Outline each Plasmodium falciparum-infected red blood cell.
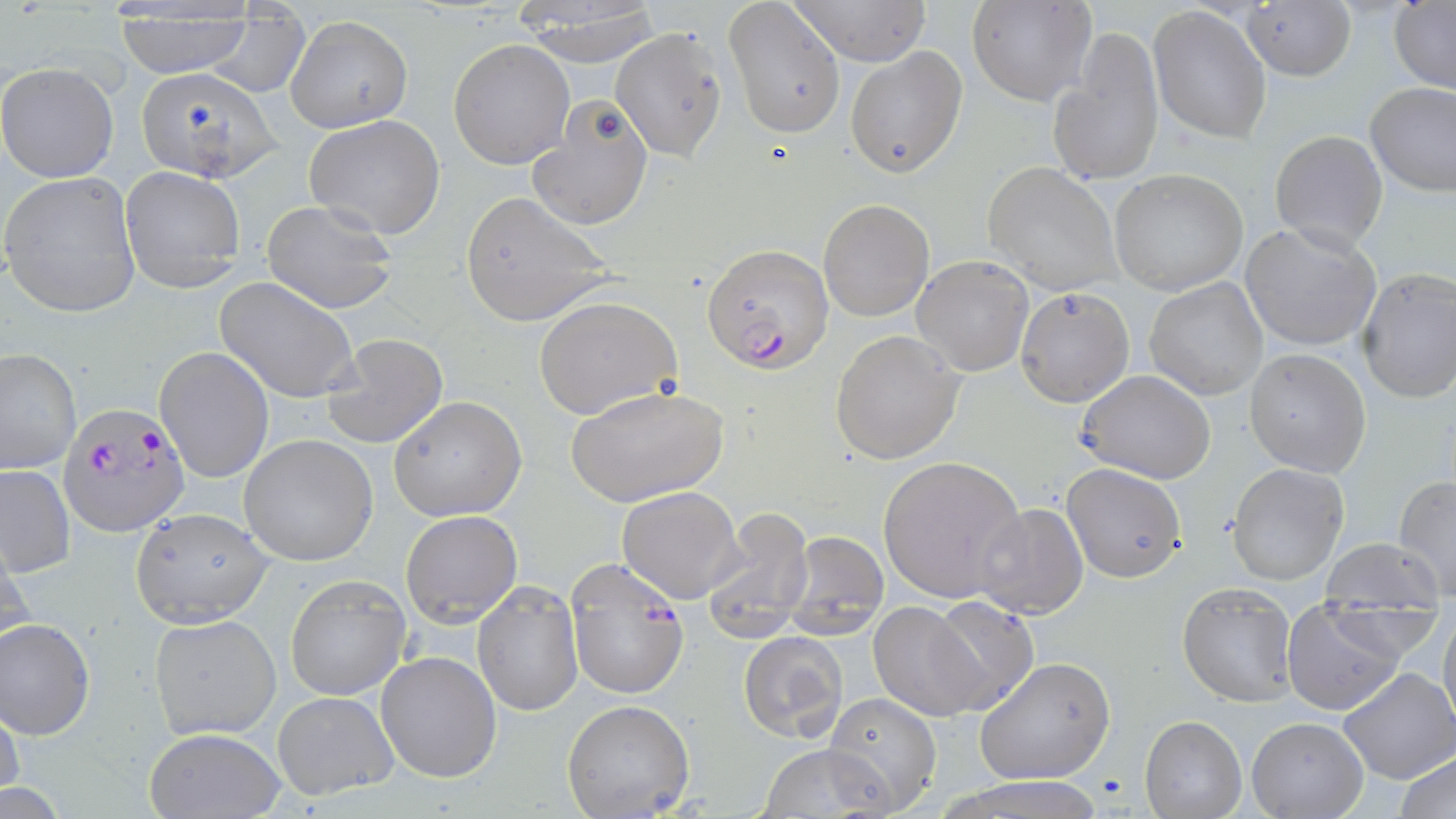

Approximate bounding boxes as (x1, y1, x2, y2) in pixels.
Plasmodium falciparum-infected red blood cells: (702, 245, 832, 372), (58, 403, 190, 537), (566, 558, 690, 699).

slide-level diagnosis = Plasmodium falciparum
image size = 1456×819 pixels
field of view = one of a larger specimen
magnification = 1000x
preparation = thin blood smear
uninfected red blood cell locations = approximate bounding boxes as (x1, y1, x2, y2) in pixels: (723, 0, 846, 135), (792, 0, 930, 64), (969, 0, 1096, 107), (1241, 0, 1356, 82), (509, 2, 667, 65), (1391, 2, 1456, 92), (1148, 4, 1272, 145), (203, 5, 311, 97), (111, 13, 256, 79), (286, 15, 412, 131), (611, 26, 729, 162), (1050, 27, 1165, 189), (449, 39, 575, 169), (844, 44, 968, 179), (1, 62, 119, 183), (137, 66, 279, 183), (1364, 81, 1456, 198), (527, 99, 654, 232), (302, 114, 447, 240), (1269, 130, 1389, 252), (982, 162, 1122, 294), (119, 166, 246, 293), (1109, 168, 1247, 296), (1, 172, 141, 318), (458, 192, 613, 326), (818, 199, 934, 321), (262, 204, 398, 298), (1241, 223, 1383, 352), (911, 255, 1034, 375), (1356, 268, 1456, 404), (215, 277, 359, 404), (1144, 277, 1269, 401), (1016, 287, 1131, 407), (535, 296, 681, 421), (829, 329, 967, 464), (324, 333, 449, 449), (0, 348, 80, 473), (156, 348, 272, 483), (1244, 348, 1370, 476), (1077, 369, 1217, 485), (565, 383, 729, 510), (389, 395, 529, 521), (239, 435, 378, 566), (877, 455, 1025, 602), (1061, 462, 1187, 584), (1229, 463, 1348, 584), (0, 465, 74, 578), (1393, 474, 1456, 600), (617, 485, 746, 602), (972, 501, 1087, 620), (129, 508, 274, 628), (699, 509, 816, 628), (400, 510, 522, 626), (782, 530, 888, 632), (1, 533, 33, 652), (1320, 538, 1442, 621), (284, 573, 412, 700), (473, 581, 583, 717), (1177, 582, 1298, 707), (921, 595, 1041, 714), (1281, 598, 1404, 716), (869, 601, 991, 722), (1439, 607, 1456, 737), (149, 613, 282, 741), (0, 618, 95, 739), (737, 631, 849, 744), (376, 651, 502, 783), (974, 656, 1116, 786), (1338, 667, 1455, 784), (271, 691, 399, 801), (823, 693, 942, 815), (562, 700, 695, 819), (0, 701, 26, 808), (1139, 715, 1248, 818), (1245, 717, 1367, 818), (143, 728, 286, 818), (758, 743, 893, 818), (1396, 751, 1456, 819), (938, 775, 1107, 819)
modality = optical microscopy
stain = May-Grünwald-Giemsa